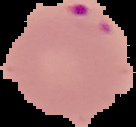

preparation = thin blood film
malaria status = parasitized
image type = segmented cell region on a black background
image size = 136×127 pixels